Comment on the morphology of the red blood cells.
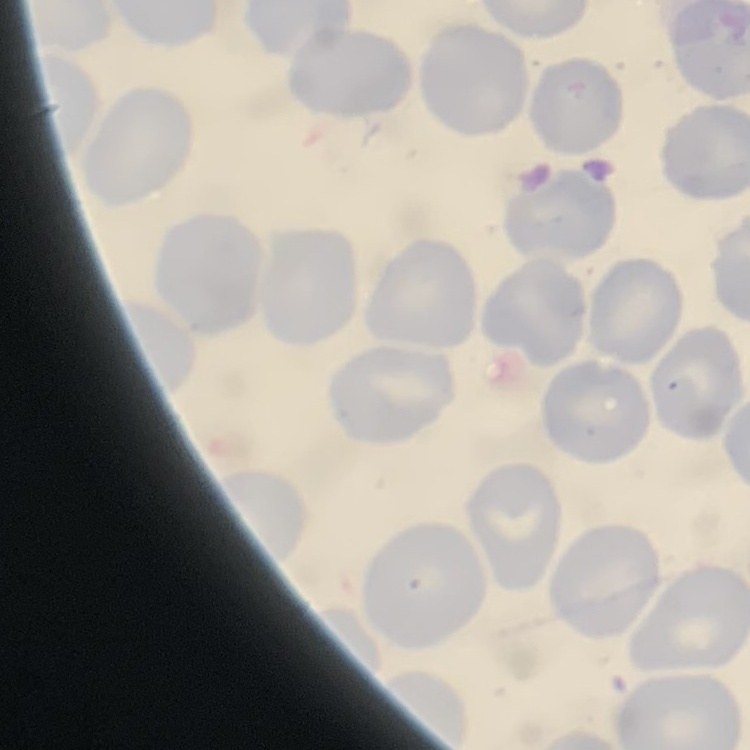
They show no rouleaux formation.

{
  "stain": "Field's or Giemsa",
  "preparation": "thin peripheral smear",
  "image_type": "square crop of a larger photomicrograph"
}